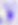

Summary:
  - Modality: micrograph
  - Identification: Toxoplasma gondii
  - Magnification: 400x